Mark where platelets are.
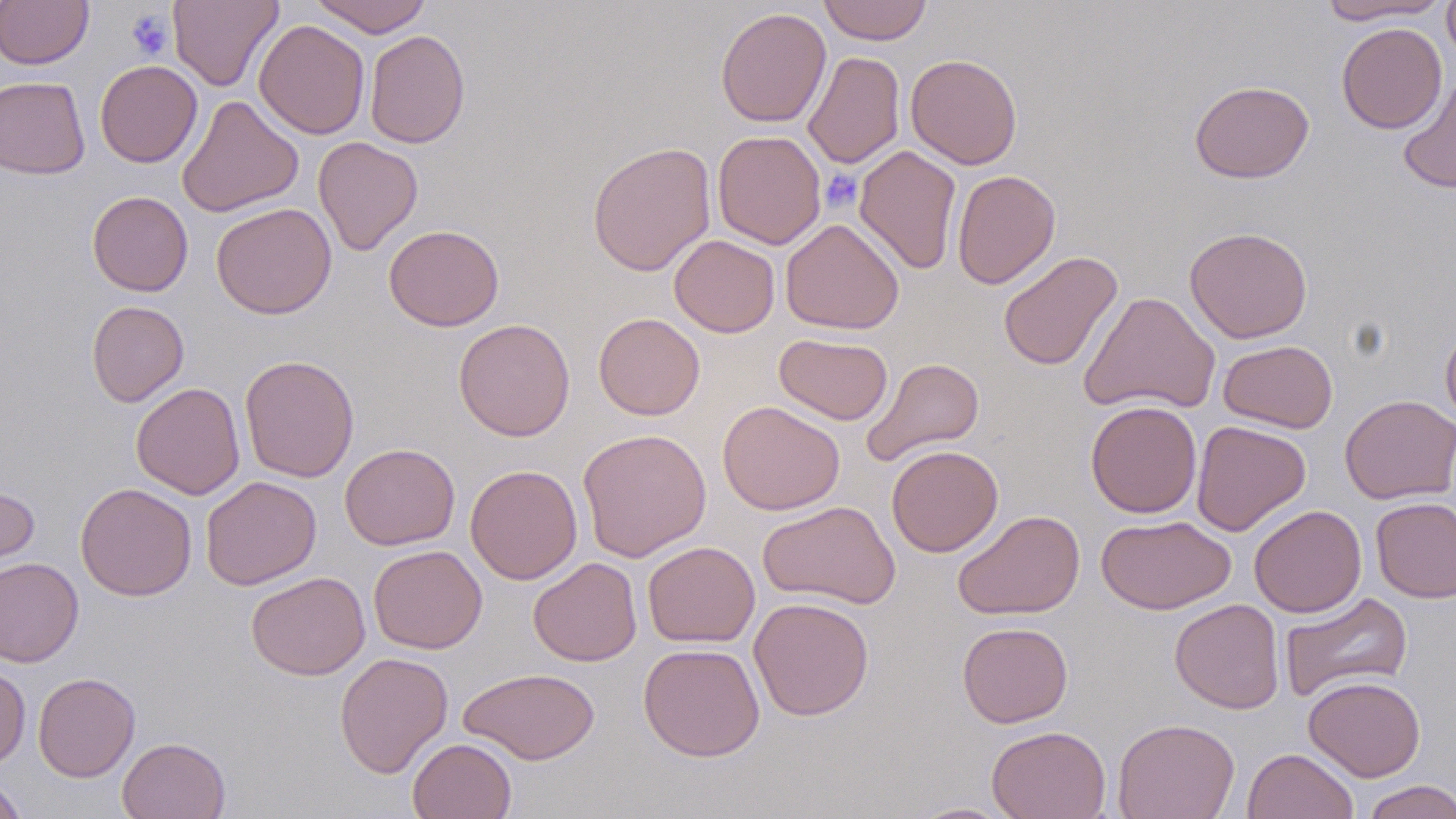

Approximate bounding boxes as (x1,y1)-(x2,y2) corner pairs in pixels.
Platelets: (126,10)-(173,60), (819,169)-(862,212).

Summary:
  - Uninfected red blood cell locations: (0,0)-(93,69), (168,0)-(283,91), (309,0)-(431,37), (818,0)-(932,45), (1316,0)-(1452,24), (1442,0)-(1456,67), (715,7)-(831,128), (254,19)-(370,140), (1336,22)-(1448,133), (365,29)-(470,149), (803,51)-(905,169), (905,53)-(1023,169), (95,60)-(202,167), (0,76)-(91,179), (1398,76)-(1456,194), (1189,80)-(1314,183), (176,95)-(304,218), (712,130)-(827,249), (313,136)-(423,256), (587,141)-(716,276), (855,145)-(962,275), (951,169)-(1060,290), (87,191)-(193,296), (211,202)-(337,319), (780,218)-(905,335), (384,224)-(504,331), (1185,226)-(1312,343), (669,234)-(780,338), (998,251)-(1123,372), (1080,291)-(1221,415), (86,301)-(189,407), (593,312)-(705,420), (454,318)-(575,441), (1440,321)-(1456,430), (774,333)-(893,425), (1218,339)-(1338,433), (240,355)-(360,483), (861,357)-(985,466), (131,382)-(245,500), (1339,395)-(1456,505), (718,400)-(845,515), (1085,400)-(1202,518), (1191,420)-(1311,535), (577,427)-(712,562), (340,443)-(460,550), (887,445)-(1003,556), (465,464)-(582,584), (201,476)-(321,590), (0,481)-(40,578), (75,482)-(197,600), (1371,496)-(1456,603), (758,500)-(901,609), (1249,504)-(1366,618), (952,510)-(1085,620), (1096,515)-(1236,614), (642,541)-(760,647), (368,545)-(487,654), (0,557)-(84,667), (528,557)-(642,666), (246,571)-(370,679), (1279,592)-(1413,703), (749,597)-(875,721), (1169,598)-(1285,714), (957,622)-(1073,728), (638,643)-(765,761), (335,651)-(453,778), (0,663)-(31,770), (459,667)-(600,764), (32,672)-(141,782), (1303,675)-(1426,782), (1113,718)-(1239,819), (986,725)-(1111,819), (116,736)-(231,819), (407,738)-(517,819), (1242,747)-(1358,819), (0,774)-(29,819), (1360,780)-(1456,819), (906,802)-(1018,818)
  - Slide-level diagnosis: no evidence of blood parasites
  - Preparation: thin blood smear
  - Modality: light microscopy
  - Image size: 1456×819 pixels
  - Field of view: single
  - Stain: May-Grünwald-Giemsa
  - Magnification: 1000x